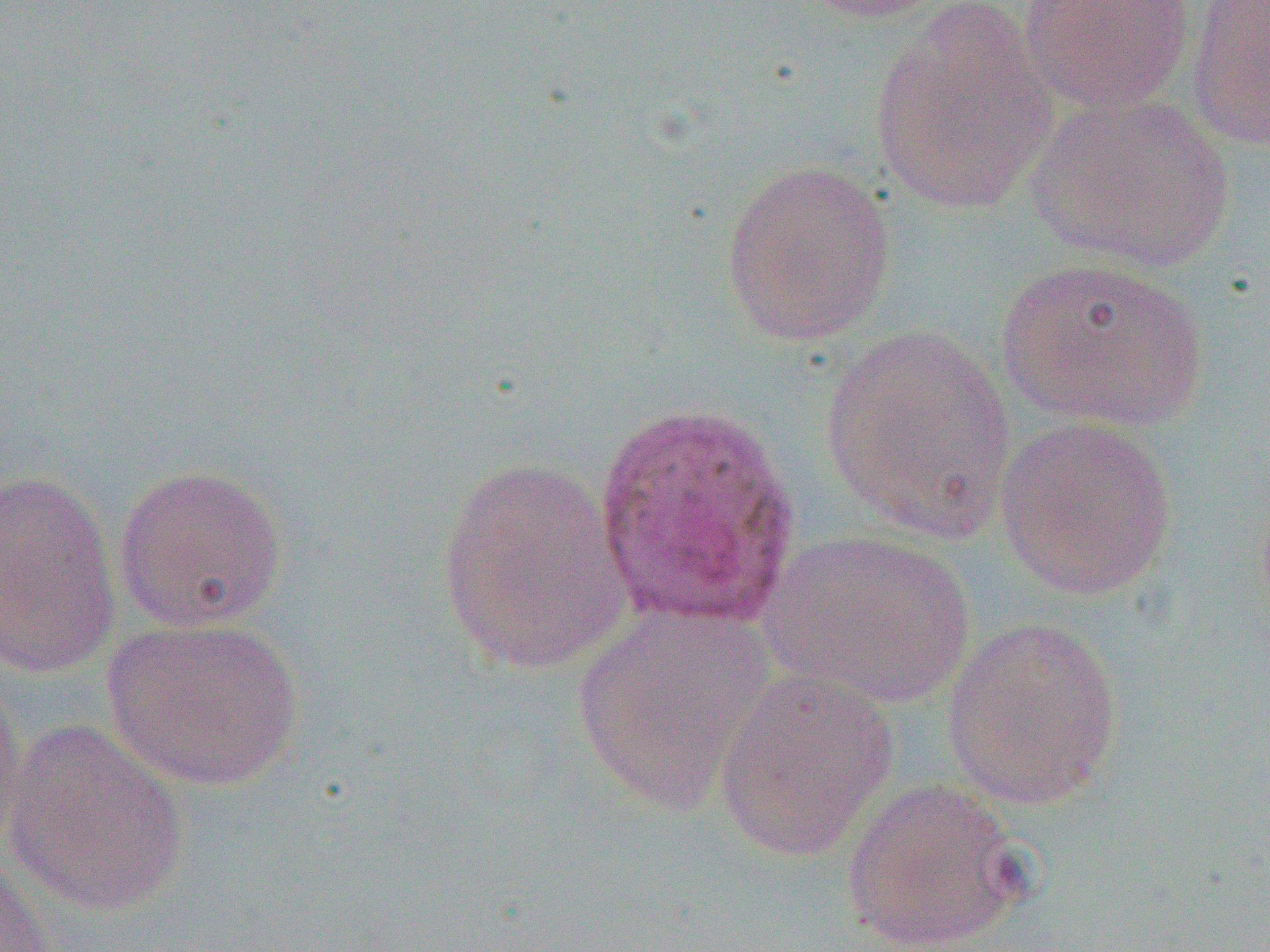

{
  "slide_level_diagnosis": "Plasmodium ovale",
  "field_of_view": "one of a larger specimen",
  "magnification": "1000x",
  "preparation": "thin blood film",
  "plasmodium_ovale_infected_red_blood_cell_locations": "approximate bounding boxes as named x1/y1/x2/y2 corners in pixels: (x1=592, y1=396, x2=804, y2=632)",
  "image_size": "1270×952 pixels",
  "uninfected_red_blood_cell_locations": "approximate bounding boxes as named x1/y1/x2/y2 corners in pixels: (x1=788, y1=0, x2=952, y2=24), (x1=1017, y1=0, x2=1197, y2=113), (x1=1187, y1=1, x2=1270, y2=153), (x1=868, y1=4, x2=1060, y2=217), (x1=1027, y1=92, x2=1238, y2=272), (x1=721, y1=158, x2=897, y2=347), (x1=995, y1=257, x2=1210, y2=432), (x1=817, y1=325, x2=1018, y2=542), (x1=995, y1=415, x2=1178, y2=601), (x1=434, y1=458, x2=635, y2=676), (x1=112, y1=463, x2=287, y2=633), (x1=0, y1=469, x2=121, y2=678), (x1=763, y1=528, x2=976, y2=711), (x1=572, y1=602, x2=777, y2=816), (x1=940, y1=615, x2=1124, y2=812), (x1=101, y1=616, x2=305, y2=792), (x1=713, y1=669, x2=900, y2=863), (x1=0, y1=672, x2=30, y2=856), (x1=1, y1=718, x2=192, y2=916), (x1=841, y1=778, x2=1026, y2=951), (x1=0, y1=860, x2=53, y2=952)",
  "modality": "optical microscopy"
}